Report the malaria status of this cell.
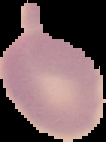
Uninfected.

Summary:
  - Preparation: thin blood film
  - Image type: segmented cell region with the area outside set to black
  - Image size: 106×142 pixels